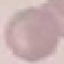

{
  "result": "negative for malaria parasites",
  "image_type": "automatically extracted cell patch, resized to 64 × 64 pixels",
  "capture": "smartphone through the microscope eyepiece",
  "preparation": "thin blood smear",
  "stain": "Giemsa"
}